Classify this cell by malaria status.
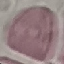

Uninfected.

Thin smear of blood. Photographed with a smartphone camera at the microscope eyepiece. Cell patch, automatically extracted from a larger field of view and resized to 64 × 64 pixels. Giemsa stain.